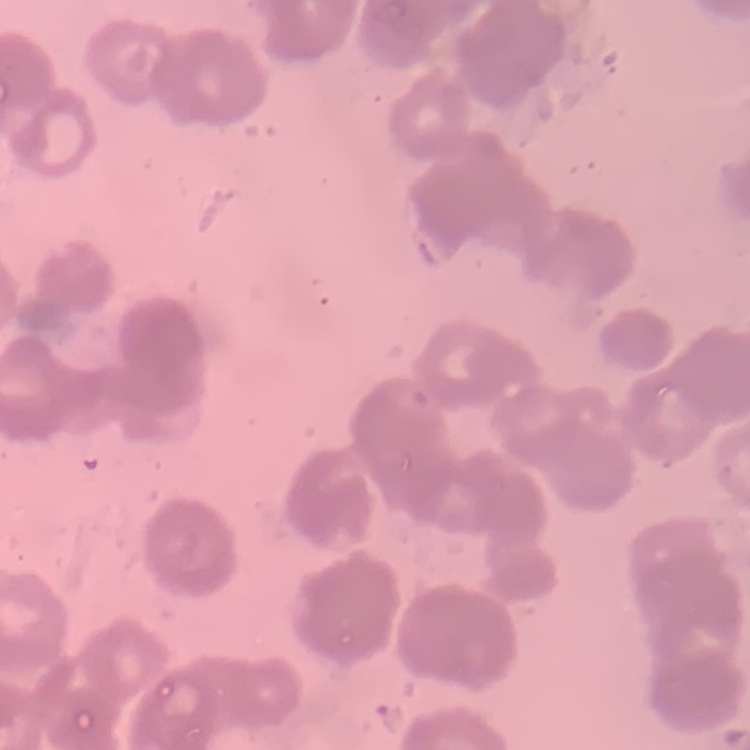
erythrocyte_morphology: rouleaux formation
image_type: square crop of a larger photomicrograph
stain: Field's or Giemsa
preparation: thin peripheral smear